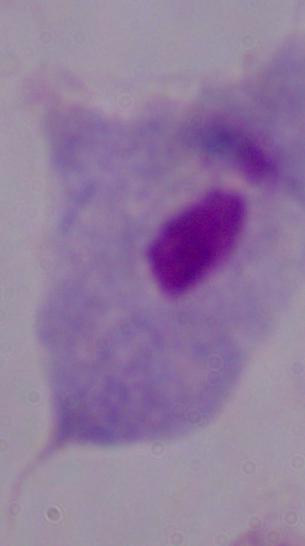

modality = photomicrograph
identification = trichomonad
magnification = 1000x